Classify this cell by malaria status.
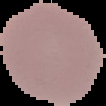

It is uninfected.

Image is 106×106 pixels. From a thin blood smear. Cell region segmented out of the field of view; the surrounding area is masked to black.